Outline each P. falciparum parasite and classify it by life-cycle stage.
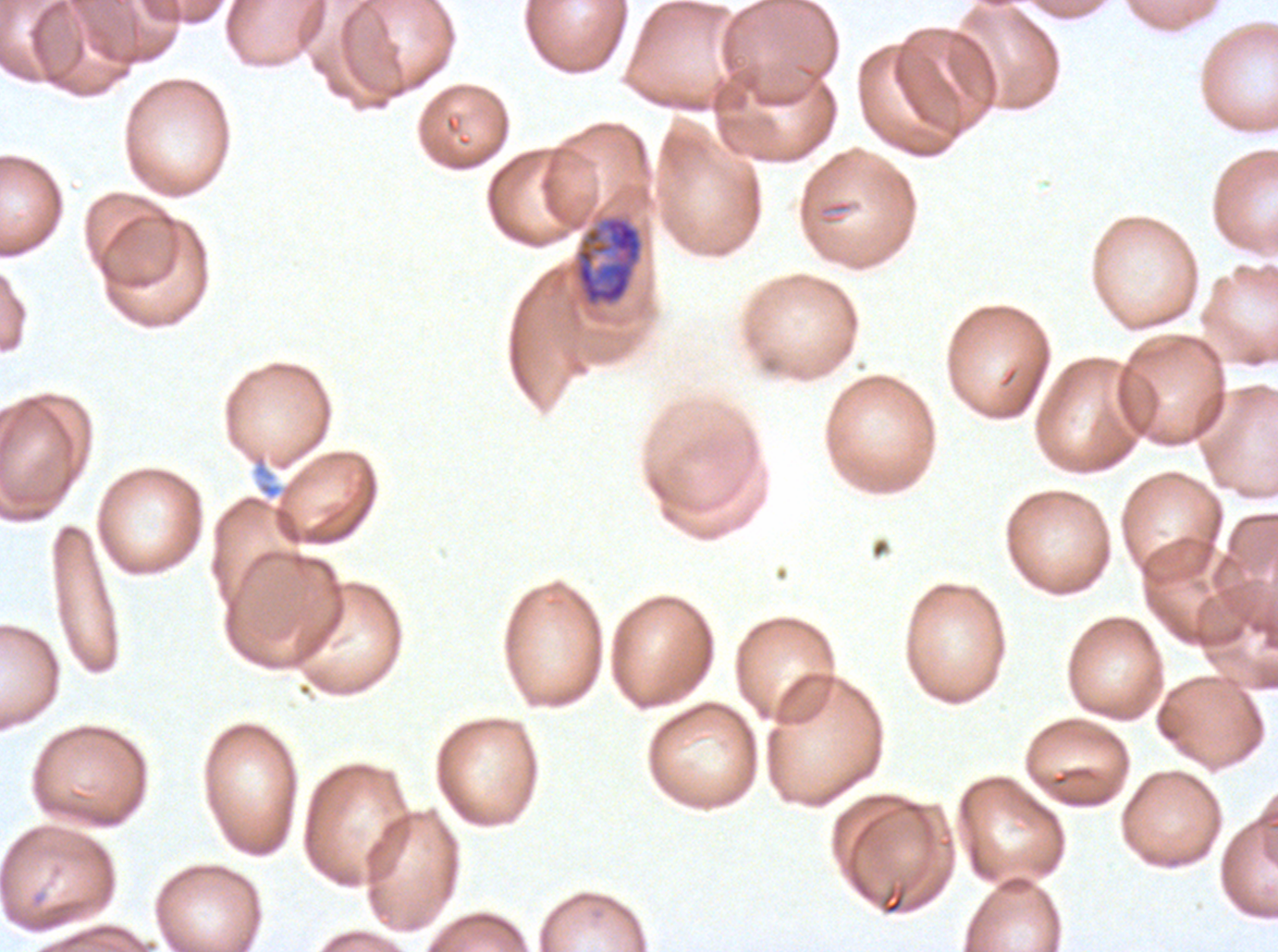

Approximate bounding boxes as [x1, y1, x2, y2] in pixels.
Early schizonts: [574, 215, 644, 307].
No rings, late-ring/early-trophozoite forms, mid trophozoites, late trophozoites, late schizonts, segmenters, or gametocytes observed.

Giemsa-stained preparation. Ex-vivo P. falciparum culture from a patient in The Gambia, grown for 24 to 48 hours. Image is 1278×952 pixels. Thin blood smear. One sub-image of a larger composite.